State which parasite is depicted.
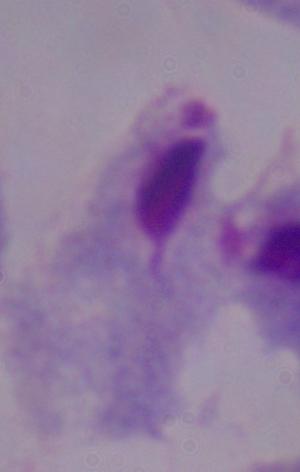

A trichomonad.

Micrograph. Captured at 1000x magnification.